Assess this cell for malaria.
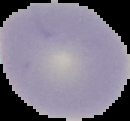
Uninfected.

Summary:
  - Preparation: thin blood smear
  - Image size: 130×121 pixels
  - Image type: segmented cell region on a black background